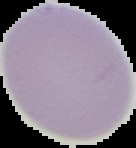
malaria status = uninfected
preparation = thin blood smear
image size = 136×148 pixels
image type = segmented cell region with the area outside set to black